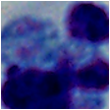

identification: white blood cell
modality: photomicrograph
magnification: 1000x